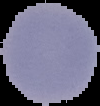

malaria status = parasitized
image size = 100×106 pixels
image type = segmented cell region on a black background
preparation = thin blood smear